Report the malaria status of this cell.
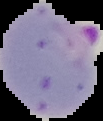

Parasitized.

{
  "image_size": "103×121 pixels",
  "image_type": "segmented cell region on a black background",
  "preparation": "thin blood film"
}